Outline each Plasmodium falciparum-infected red blood cell.
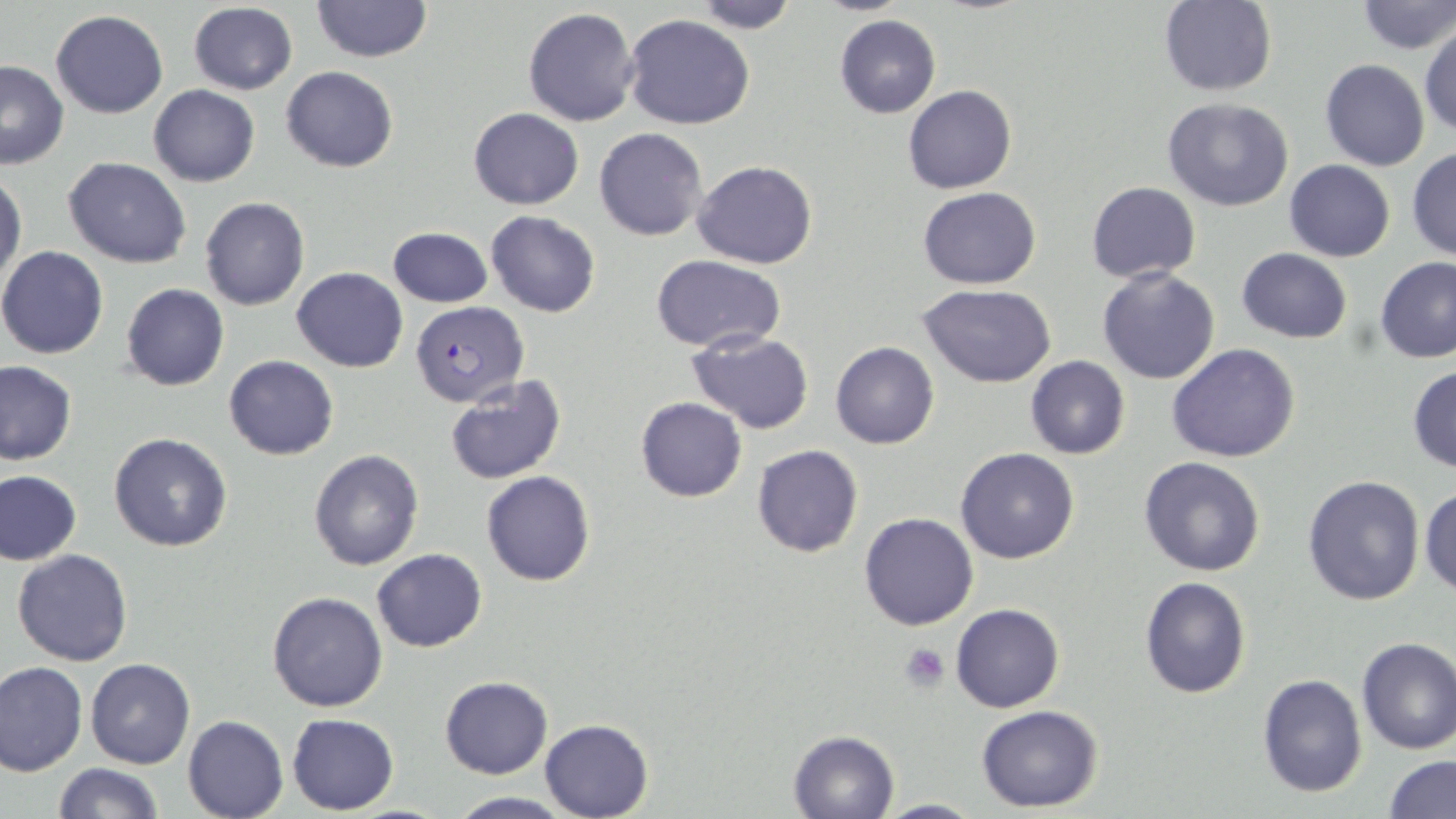
Approximate bounding boxes as [x1, y1, x2, y2] in pixels.
Plasmodium falciparum-infected red blood cells: [409, 301, 528, 407].

{
  "slide_level_diagnosis": "Plasmodium falciparum",
  "platelet_locations": "approximate bounding boxes as [x1, y1, x2, y2] in pixels: [901, 642, 950, 693]",
  "preparation": "thin blood film",
  "stain": "May-Grünwald-Giemsa",
  "field_of_view": "one of a larger specimen",
  "magnification": "1000x",
  "uninfected_red_blood_cell_locations": "approximate bounding boxes as [x1, y1, x2, y2] in pixels: [690, 0, 801, 33], [1159, 0, 1277, 95], [309, 1, 433, 63], [1354, 1, 1455, 55], [187, 2, 298, 94], [524, 7, 639, 127], [51, 8, 168, 119], [623, 14, 755, 130], [834, 15, 941, 118], [1419, 22, 1455, 139], [1320, 59, 1429, 171], [0, 60, 69, 167], [281, 67, 398, 172], [149, 85, 260, 187], [903, 85, 1017, 194], [1162, 98, 1293, 210], [469, 107, 584, 210], [595, 128, 707, 242], [1407, 147, 1456, 261], [64, 157, 191, 269], [1285, 159, 1396, 262], [694, 161, 818, 269], [0, 169, 25, 294], [1087, 181, 1201, 282], [917, 187, 1042, 290], [200, 197, 310, 311], [486, 211, 600, 317], [388, 227, 491, 308], [0, 246, 108, 359], [1235, 247, 1354, 342], [1375, 255, 1456, 363], [650, 256, 787, 352], [1097, 266, 1221, 385], [292, 267, 407, 374], [916, 282, 1056, 387], [122, 284, 229, 391], [685, 331, 814, 433], [831, 342, 939, 449], [1166, 344, 1299, 463], [223, 355, 338, 459], [1024, 356, 1131, 459], [0, 360, 77, 465], [1407, 364, 1456, 474], [443, 374, 568, 485], [635, 397, 746, 502], [110, 433, 234, 553], [752, 444, 863, 558], [955, 447, 1080, 564], [309, 449, 424, 572], [1137, 455, 1266, 578], [0, 470, 83, 566], [481, 470, 596, 586], [1302, 474, 1427, 608], [1419, 485, 1456, 597], [859, 512, 979, 630], [11, 548, 133, 666], [372, 548, 487, 651], [1138, 577, 1251, 698], [266, 590, 388, 712], [950, 603, 1065, 713], [1354, 636, 1456, 754], [85, 658, 196, 769], [0, 660, 88, 776], [1256, 672, 1367, 798], [440, 676, 553, 779], [975, 705, 1103, 813], [287, 714, 398, 814], [183, 715, 289, 819], [540, 718, 653, 819], [787, 729, 900, 819], [1383, 754, 1456, 819], [53, 763, 164, 819], [446, 792, 574, 818], [876, 797, 983, 817]",
  "image_size": "1456×819 pixels",
  "modality": "optical microscopy"
}